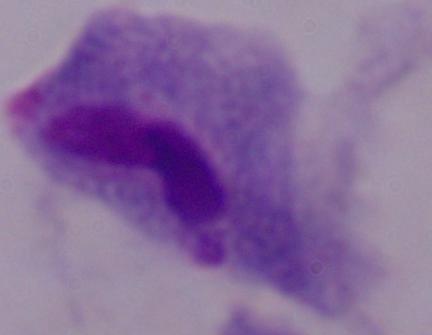

identification: trichomonad
modality: micrograph
magnification: 1000x